Describe the morphology of the red blood cells.
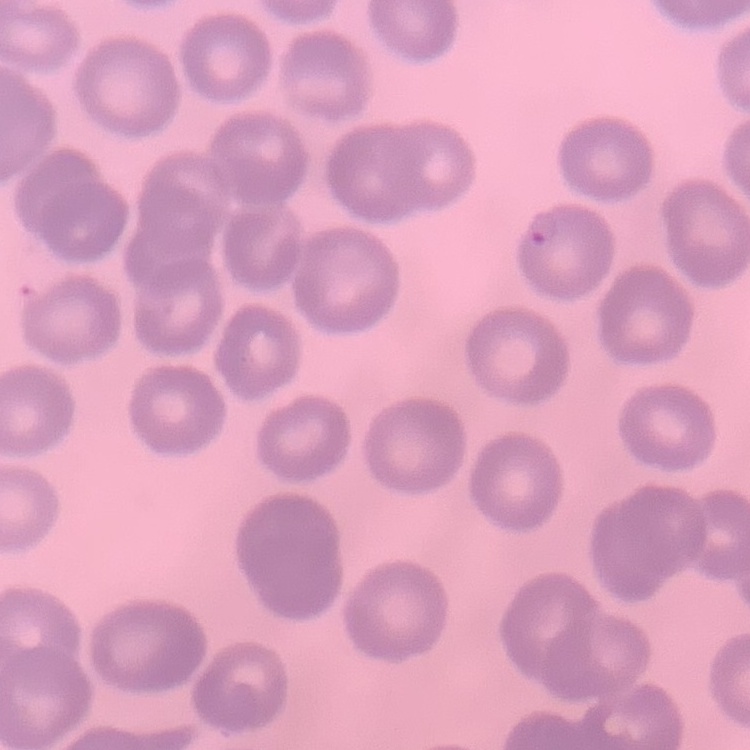

They show no rouleaux formation.

Thin blood film. Field's or Giemsa stain. Square crop of a larger photomicrograph.